Identify the cell.
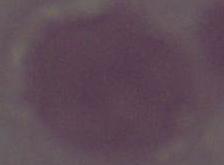

This is an erythrocyte.

Summary:
  - Magnification: 1000x
  - Modality: micrograph